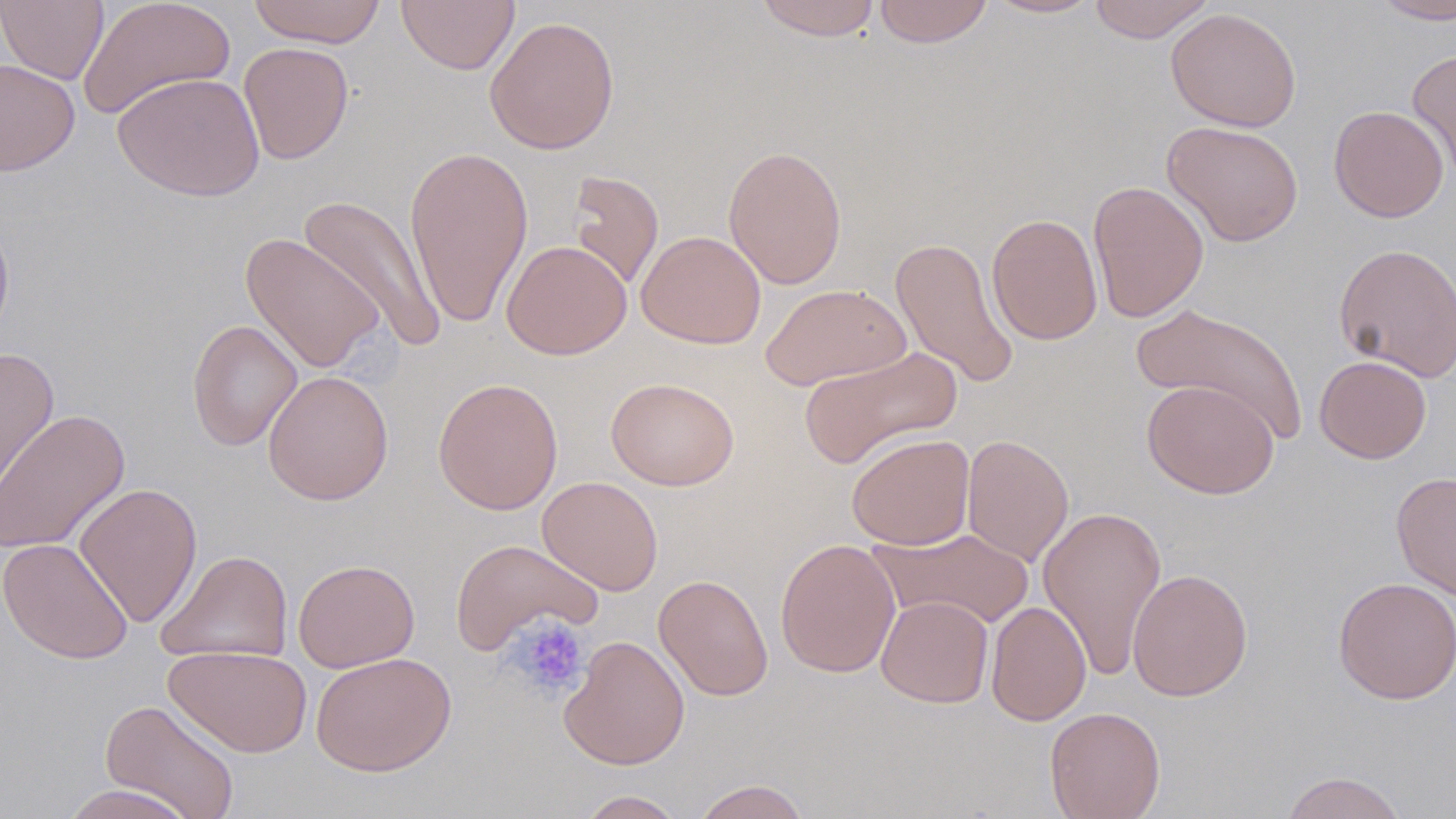

{
  "slide_level_diagnosis": "negative for blood parasites",
  "modality": "optical microscopy",
  "image_size": "1456×819 pixels",
  "field_of_view": "single",
  "magnification": "1000x",
  "stain": "May-Grünwald-Giemsa",
  "platelet_locations": "approximate bounding boxes as named x1/y1/x2/y2 corners in pixels: (x1=507, y1=616, x2=590, y2=699)",
  "uninfected_red_blood_cell_locations": "approximate bounding boxes as named x1/y1/x2/y2 corners in pixels: (x1=0, y1=0, x2=109, y2=85), (x1=78, y1=0, x2=236, y2=122), (x1=246, y1=0, x2=386, y2=48), (x1=396, y1=0, x2=520, y2=74), (x1=754, y1=0, x2=882, y2=40), (x1=873, y1=0, x2=994, y2=48), (x1=981, y1=0, x2=1105, y2=19), (x1=1087, y1=0, x2=1215, y2=43), (x1=1370, y1=0, x2=1456, y2=24), (x1=1165, y1=8, x2=1302, y2=132), (x1=484, y1=15, x2=620, y2=155), (x1=238, y1=42, x2=354, y2=164), (x1=1407, y1=48, x2=1456, y2=181), (x1=0, y1=58, x2=80, y2=176), (x1=112, y1=72, x2=265, y2=202), (x1=1328, y1=105, x2=1449, y2=223), (x1=1161, y1=120, x2=1305, y2=247), (x1=404, y1=144, x2=534, y2=329), (x1=723, y1=144, x2=848, y2=289), (x1=565, y1=169, x2=665, y2=293), (x1=1087, y1=179, x2=1209, y2=323), (x1=299, y1=194, x2=448, y2=353), (x1=987, y1=213, x2=1103, y2=346), (x1=0, y1=214, x2=15, y2=347), (x1=635, y1=230, x2=766, y2=349), (x1=240, y1=233, x2=386, y2=373), (x1=889, y1=235, x2=1019, y2=391), (x1=501, y1=240, x2=631, y2=360), (x1=1332, y1=241, x2=1456, y2=384), (x1=760, y1=283, x2=911, y2=391), (x1=1134, y1=302, x2=1307, y2=443), (x1=187, y1=318, x2=303, y2=452), (x1=798, y1=346, x2=963, y2=470), (x1=0, y1=348, x2=59, y2=502), (x1=1314, y1=355, x2=1432, y2=463), (x1=262, y1=370, x2=394, y2=505), (x1=432, y1=377, x2=563, y2=515), (x1=605, y1=377, x2=739, y2=491), (x1=1142, y1=379, x2=1279, y2=499), (x1=0, y1=409, x2=131, y2=554), (x1=846, y1=433, x2=975, y2=550), (x1=961, y1=434, x2=1074, y2=568), (x1=1391, y1=471, x2=1456, y2=600), (x1=537, y1=475, x2=663, y2=596), (x1=74, y1=482, x2=203, y2=629), (x1=1037, y1=505, x2=1168, y2=679), (x1=870, y1=527, x2=1035, y2=630), (x1=0, y1=538, x2=134, y2=665), (x1=450, y1=538, x2=602, y2=655), (x1=775, y1=538, x2=901, y2=678), (x1=155, y1=549, x2=293, y2=664), (x1=293, y1=558, x2=420, y2=673), (x1=1127, y1=568, x2=1253, y2=701), (x1=653, y1=573, x2=774, y2=702), (x1=1334, y1=576, x2=1455, y2=705), (x1=876, y1=595, x2=994, y2=708), (x1=986, y1=600, x2=1091, y2=727), (x1=559, y1=635, x2=690, y2=770), (x1=163, y1=645, x2=312, y2=757), (x1=311, y1=652, x2=457, y2=776), (x1=100, y1=698, x2=240, y2=818), (x1=1044, y1=707, x2=1166, y2=818), (x1=1279, y1=770, x2=1409, y2=819), (x1=691, y1=779, x2=812, y2=819), (x1=58, y1=783, x2=198, y2=819), (x1=576, y1=790, x2=686, y2=819)",
  "preparation": "thin blood smear"
}